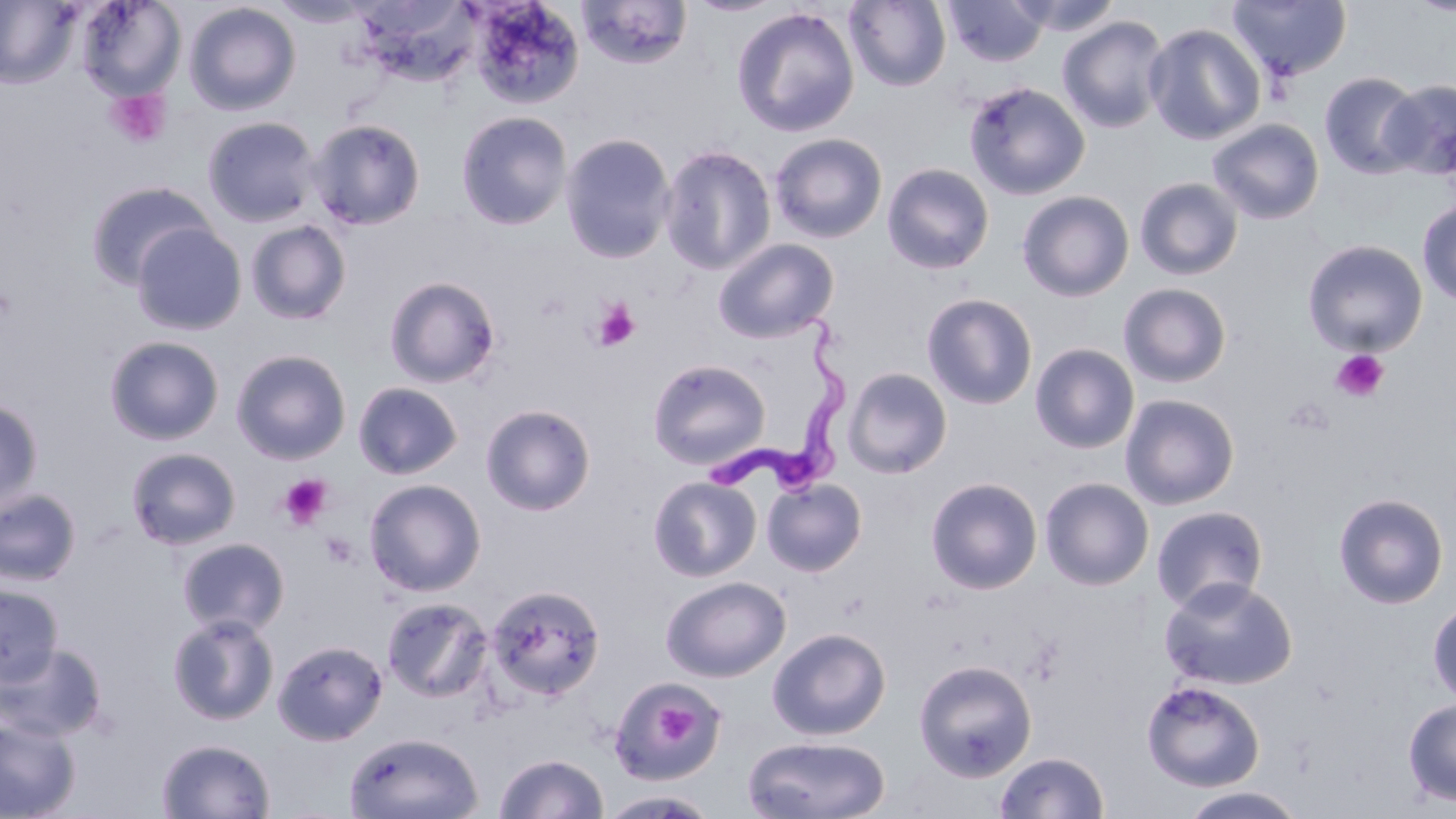
Approximate bounding boxes as (x1, y1, x2, y2) in pixels. Trypanosoma brucei locations: (698, 307, 854, 505). Uninfected red blood cell locations: (0, 0, 81, 89), (76, 0, 185, 100), (268, 0, 376, 27), (466, 0, 586, 110), (577, 0, 693, 70), (685, 0, 787, 17), (943, 0, 1051, 67), (1007, 0, 1122, 36), (1226, 0, 1352, 83), (1406, 0, 1456, 17), (844, 1, 951, 91), (183, 2, 301, 116), (354, 2, 483, 87), (731, 7, 860, 138), (1057, 16, 1172, 134), (1143, 23, 1267, 146), (1319, 72, 1424, 179), (1380, 79, 1456, 180), (963, 81, 1091, 200), (455, 111, 573, 230), (202, 116, 321, 227), (307, 118, 427, 231), (1207, 118, 1324, 225), (559, 132, 676, 264), (769, 132, 888, 243), (659, 144, 777, 275), (881, 163, 995, 275), (1134, 177, 1244, 281), (84, 180, 216, 290), (1017, 190, 1134, 302), (1417, 200, 1456, 305), (244, 218, 352, 326), (131, 222, 247, 336), (712, 238, 839, 344), (1302, 239, 1428, 357), (383, 276, 502, 388), (1118, 283, 1232, 388), (921, 293, 1038, 410), (103, 335, 225, 446), (1030, 343, 1139, 454), (231, 348, 352, 465), (647, 359, 771, 469), (842, 368, 953, 479), (353, 381, 462, 480), (1120, 393, 1240, 510), (0, 397, 44, 515), (481, 404, 596, 516), (125, 447, 242, 550), (648, 475, 761, 582), (925, 477, 1043, 594), (1039, 477, 1154, 591), (762, 478, 867, 577), (363, 479, 486, 596), (0, 488, 82, 587), (1333, 492, 1449, 609), (1151, 505, 1269, 614), (178, 537, 290, 636), (661, 576, 791, 682), (1159, 577, 1298, 691), (0, 584, 64, 686), (486, 584, 605, 700), (381, 597, 494, 703), (1427, 598, 1456, 707), (167, 614, 280, 726), (767, 627, 891, 740), (273, 639, 388, 745), (0, 643, 107, 742), (914, 659, 1038, 782), (609, 676, 726, 786), (1141, 680, 1265, 792), (1402, 697, 1456, 807), (0, 715, 80, 818), (344, 731, 484, 819), (742, 735, 892, 819), (156, 738, 276, 818), (994, 751, 1109, 818), (494, 753, 608, 818), (1177, 786, 1308, 819), (599, 790, 719, 818). Platelet locations: (105, 89, 171, 150), (592, 299, 641, 351), (1330, 349, 1390, 404), (1284, 397, 1335, 436), (279, 474, 333, 530), (319, 531, 359, 568), (654, 692, 702, 744). Slide-level diagnosis: Trypanosoma brucei. Optical microscopy. Thin blood film. May-Grünwald-Giemsa-stained preparation. Image is 1456×819 pixels. 1000x magnification. Single field of view.